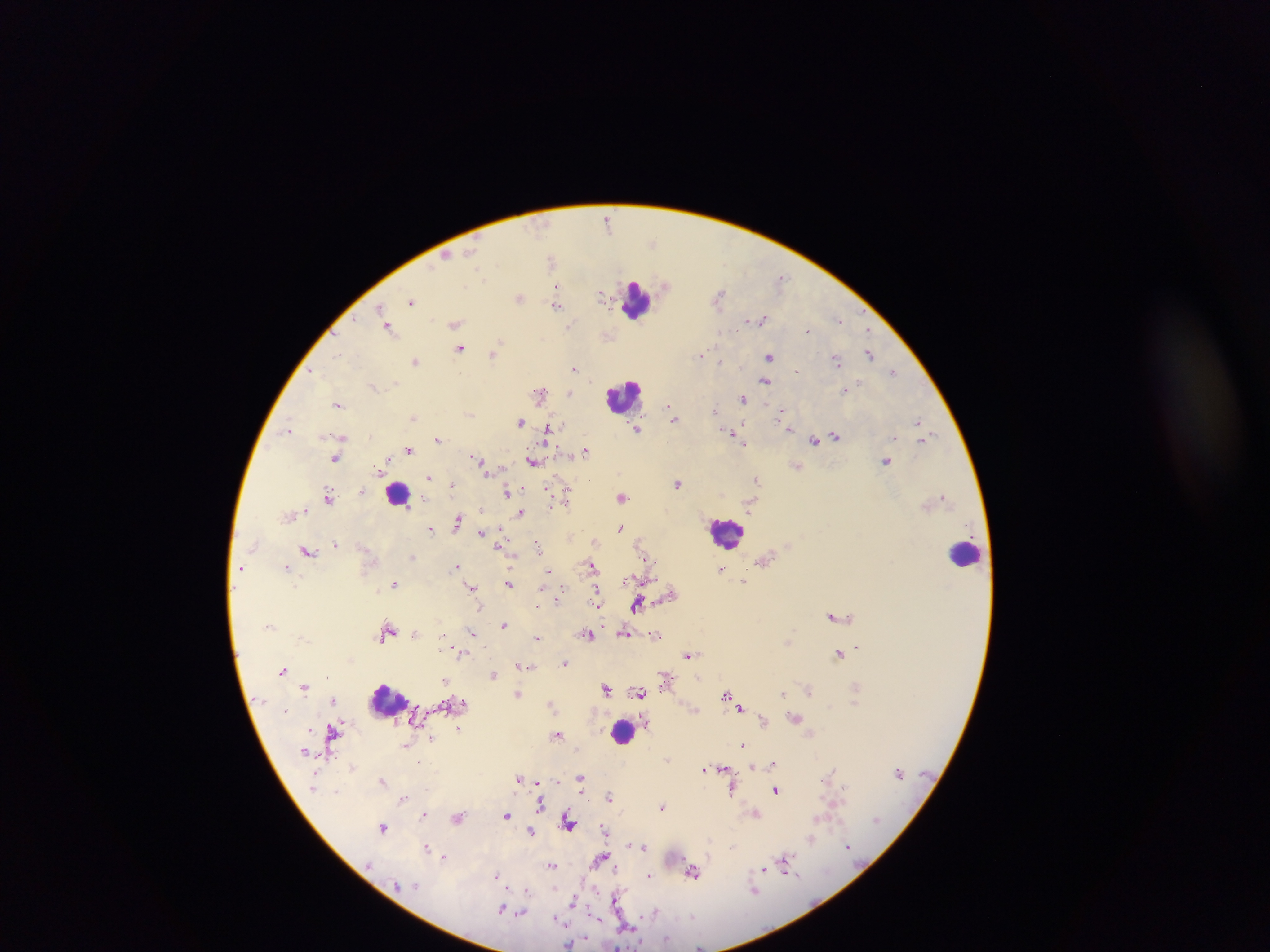
Approximate centers as (x, y) in pixels. Leukocyte locations: (637, 300), (624, 396), (398, 494), (726, 534), (965, 554), (387, 699), (623, 732). Plasmodium parasite locations: (607, 220), (652, 242), (446, 256), (551, 259), (780, 278), (665, 286), (556, 287), (600, 294), (719, 295), (519, 297), (412, 301), (556, 305), (381, 310), (839, 319), (762, 320), (455, 323), (569, 327), (390, 329), (807, 331), (868, 331), (459, 348), (339, 353), (494, 353), (701, 353), (870, 354), (769, 356), (836, 360), (415, 361), (721, 363), (575, 368), (797, 370), (893, 372), (313, 373), (766, 381), (855, 385), (847, 390), (540, 393), (569, 393), (742, 400), (338, 405), (670, 408), (715, 409), (780, 413), (674, 416), (413, 417), (519, 421), (919, 421), (786, 427), (921, 427), (289, 428), (637, 429), (548, 432), (732, 433), (895, 436), (342, 437), (835, 437), (924, 438), (438, 439), (815, 440), (742, 442), (410, 450), (586, 451), (335, 458), (479, 461), (532, 461), (886, 462), (797, 466), (380, 469), (429, 478), (757, 478), (677, 483), (453, 485), (507, 492), (567, 492), (329, 495), (944, 496), (622, 497), (550, 507), (522, 512), (457, 522), (620, 528), (430, 529), (481, 534), (594, 542), (336, 544), (538, 546), (307, 551), (644, 552), (457, 566), (592, 566), (286, 567), (721, 569), (549, 571), (639, 580), (745, 581), (509, 583), (394, 584), (471, 587), (671, 592), (560, 596), (596, 601), (637, 605), (833, 616), (503, 625), (388, 631), (415, 633), (472, 633), (624, 633), (589, 634), (655, 635), (538, 638), (857, 646), (454, 649), (689, 654), (839, 655), (565, 663), (521, 666), (283, 670), (494, 674), (664, 677), (445, 680), (305, 688), (605, 688), (856, 688), (809, 689), (640, 693), (784, 693), (518, 694), (727, 695), (333, 701), (552, 703), (741, 708), (795, 718), (762, 721), (459, 728), (332, 733), (557, 734), (432, 738), (742, 744), (407, 745), (667, 758), (772, 763), (753, 765), (352, 767), (723, 769), (703, 770), (830, 773), (580, 778), (519, 779), (383, 781), (539, 785), (732, 789), (776, 790), (336, 791), (610, 796), (403, 799), (540, 804), (662, 807), (424, 814), (755, 814), (506, 816), (459, 818), (568, 821), (382, 827), (604, 828), (532, 831), (811, 838), (629, 844), (643, 846), (848, 846), (426, 848), (444, 857), (601, 859), (785, 864), (552, 865), (763, 869), (692, 871), (497, 875), (649, 876), (755, 891), (526, 893), (573, 900), (615, 900), (503, 909), (523, 911), (655, 912), (692, 915), (630, 927), (667, 940), (570, 943). Photographed through a microscope with a mobile-phone camera. Sample from Ghana. Image is 1270×952 pixels. Thick blood film. One field of view.